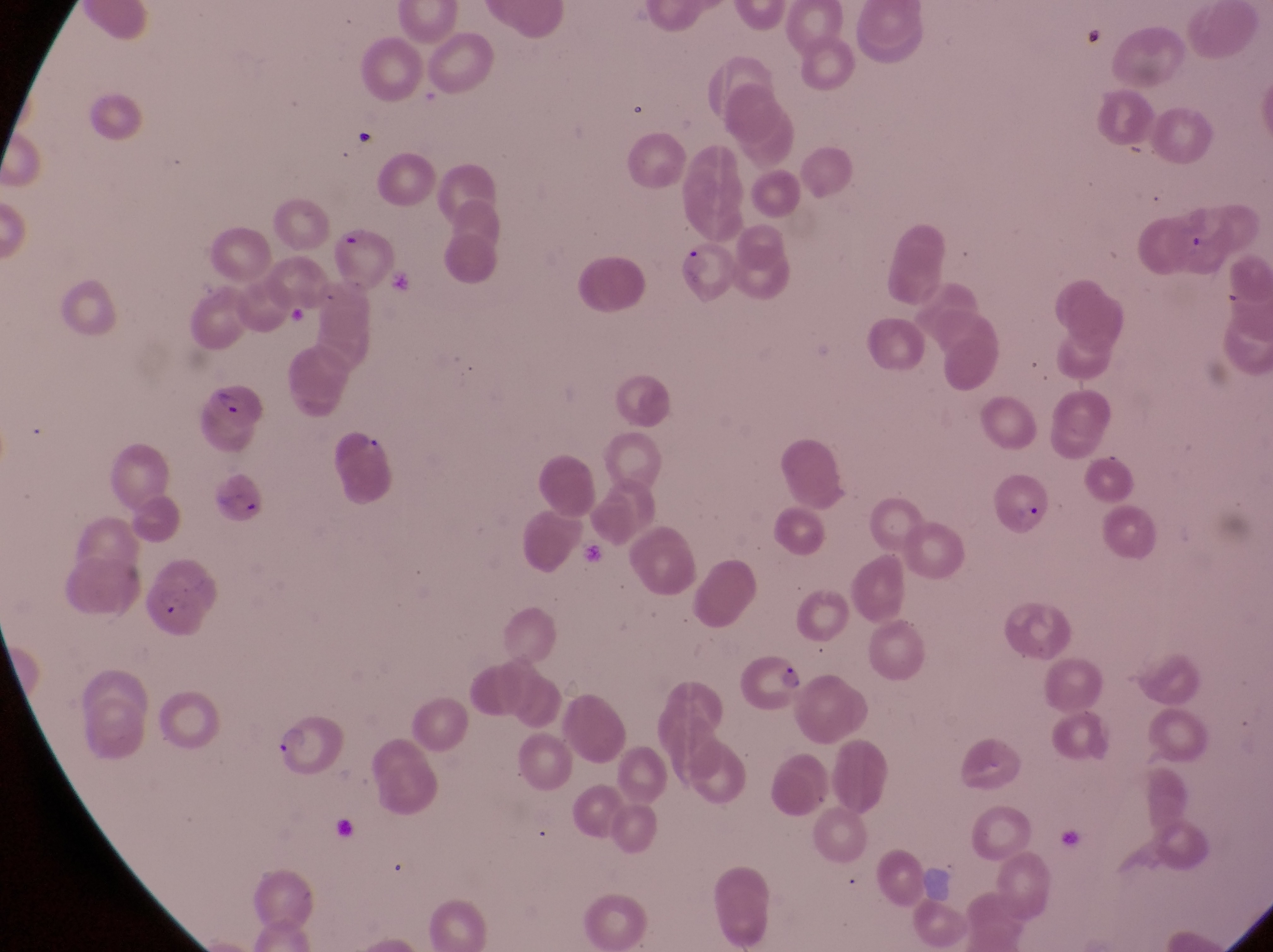

field of view = single
magnification = 1000x
parasitised red blood cell locations = approximate bounding boxes as {left, top, right, bottom} in pixels: {330, 223, 397, 283}, {679, 235, 746, 298}, {199, 380, 269, 438}, {210, 460, 272, 535}, {995, 472, 1058, 539}, {136, 571, 220, 640}, {731, 642, 805, 714}, {270, 719, 344, 781}
preparation = thin blood smear
country = Uganda
capture = smartphone photograph through the eyepiece of an Olympus CX-23 microscope
image size = 1273×952 pixels